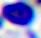 Micrograph. A leukocyte is seen. 400x magnification.